Point out each Plasmodium parasite.
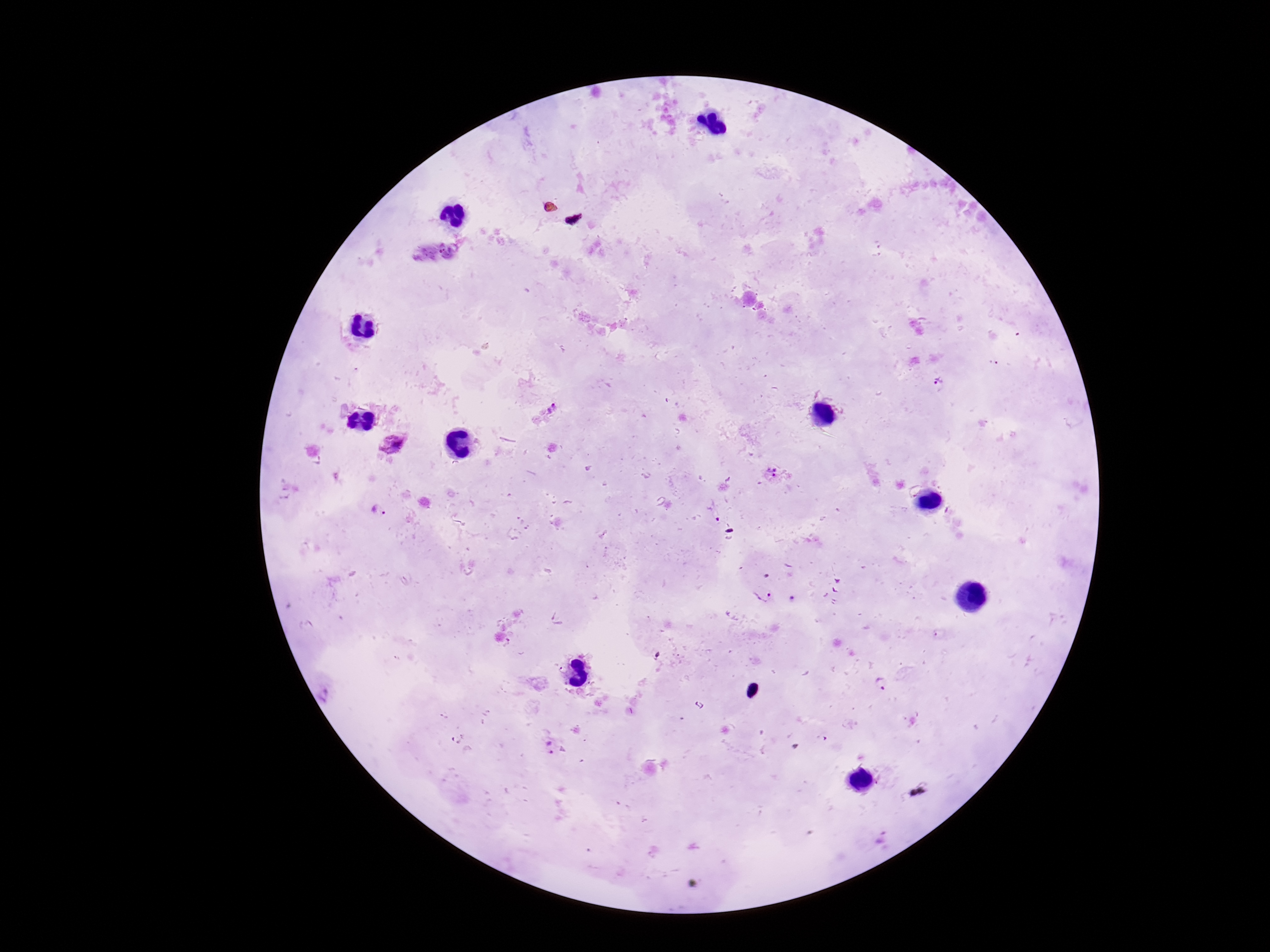

Approximate centers as {x, y} in pixels.
Plasmodium parasites: {993, 364}, {940, 383}, {552, 410}, {393, 445}, {771, 472}, {378, 509}, {761, 595}, {791, 599}, {884, 684}, {331, 692}, {549, 747}, {882, 837}.

Smartphone photograph taken through the microscope eyepiece. Image is 1270×952 pixels. Thick peripheral-blood smear. 100x magnification. Giemsa stain. Patient malaria status: infected. One field from this slide.